Point out each Plasmodium parasite.
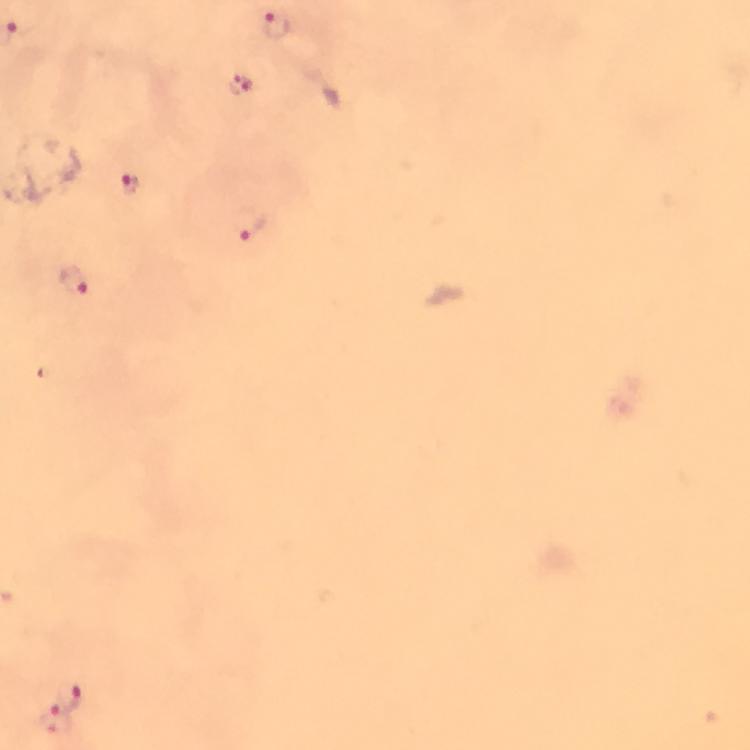
Approximate centers as (x, y) in pixels.
Plasmodium parasites: (277, 24), (240, 85), (128, 184), (251, 223), (71, 282), (73, 692), (62, 707), (56, 723).

{
  "context": "from a diagnostic examination for malaria",
  "magnification": "100x",
  "cropped_from": "a single field of view",
  "immersion_oil": "used",
  "stain": "Giemsa",
  "preparation": "thick blood film",
  "capture": "smartphone camera through the microscope",
  "image_size": "750×750 pixels"
}